Identify the cell.
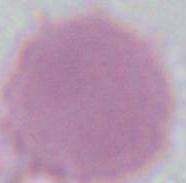

This is an erythrocyte.

modality = micrograph
magnification = 1000x